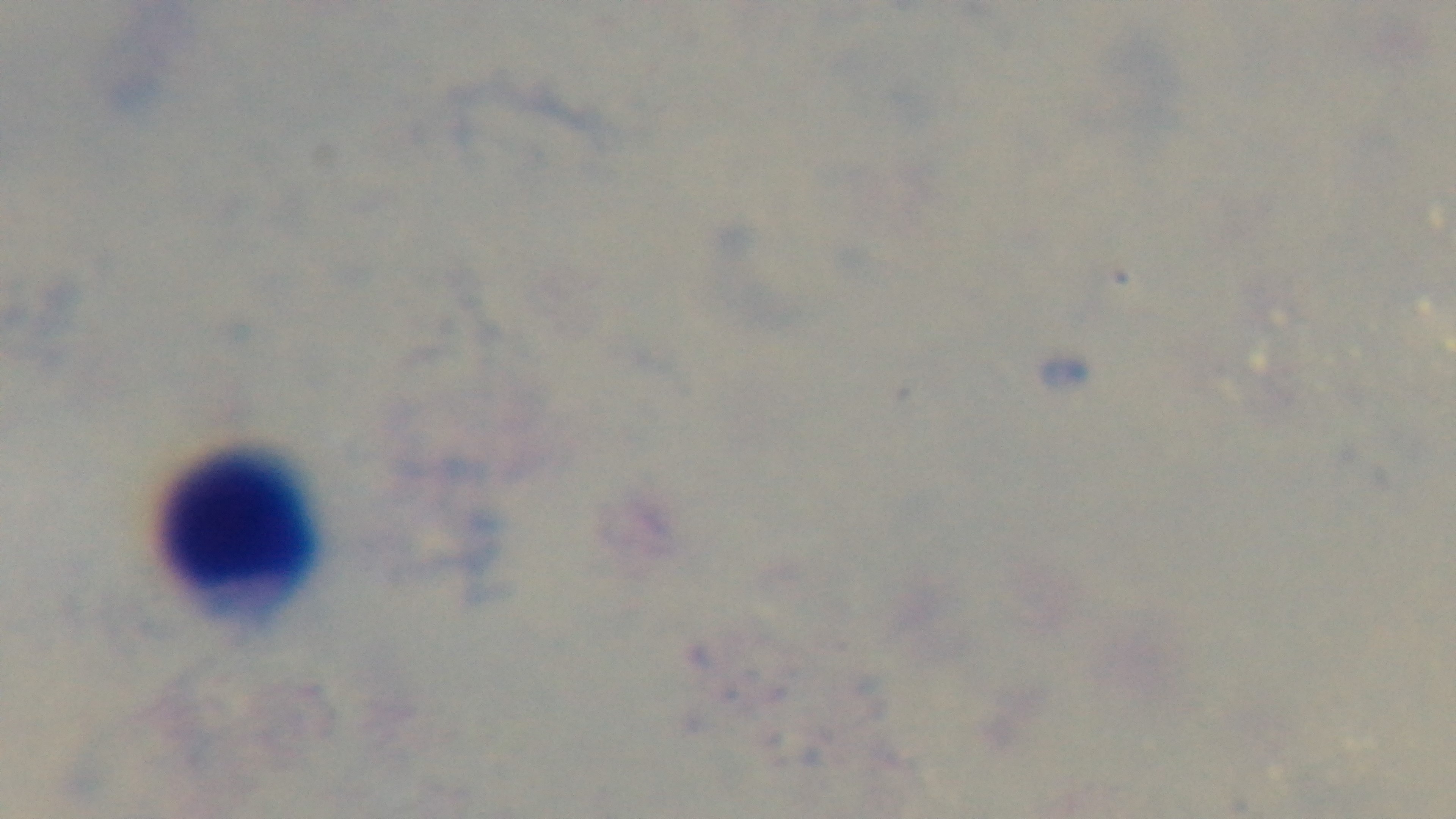
stain = Giemsa
objective = 100x oil immersion
preparation = thick
malaria status = negative
capture = mounted 4K digital camera
modality = light microscopy
field of view = single